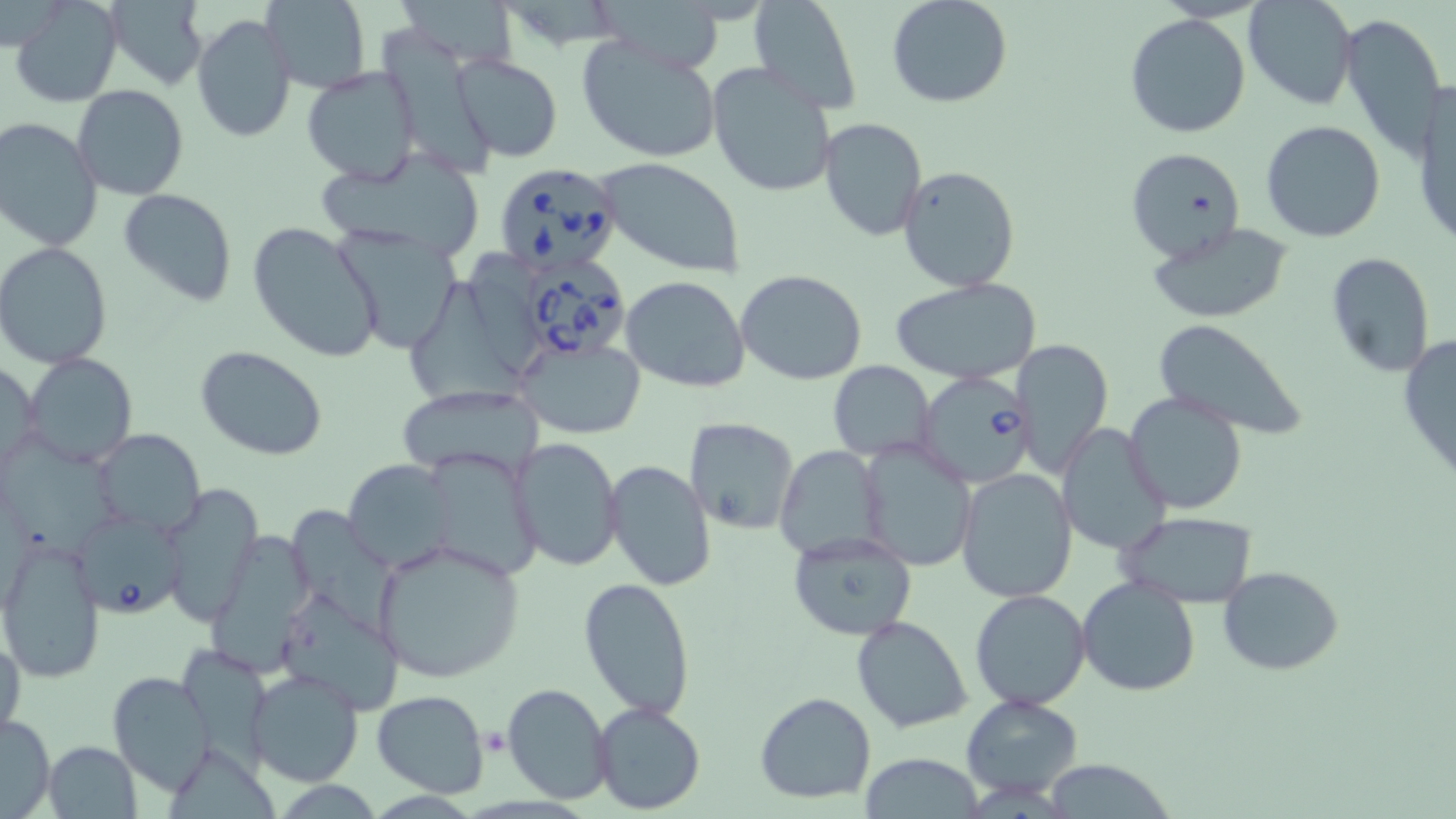
Babesia divergens-infected red blood cell locations = approximate bounding boxes as [x1, y1, x2, y2] in pixels: [493, 162, 625, 274], [521, 256, 638, 365], [914, 372, 1035, 489], [72, 511, 187, 619]
slide-level diagnosis = Babesia divergens
magnification = 1000x
image size = 1456×819 pixels
field of view = single
preparation = thin blood film
stain = May-Grünwald-Giemsa
uninfected red blood cell locations = approximate bounding boxes as [x1, y1, x2, y2] in pixels: [10, 0, 123, 107], [105, 0, 208, 90], [262, 0, 371, 94], [887, 0, 1013, 108], [1243, 1, 1357, 110], [749, 2, 861, 115], [600, 5, 725, 75], [1124, 12, 1252, 140], [1339, 12, 1446, 160], [191, 13, 296, 143], [383, 29, 499, 176], [577, 36, 723, 165], [450, 54, 562, 164], [707, 62, 838, 199], [300, 66, 421, 187], [1413, 80, 1455, 252], [72, 86, 190, 201], [0, 117, 104, 252], [819, 117, 927, 243], [1262, 119, 1385, 243], [1127, 146, 1246, 265], [314, 149, 489, 260], [598, 159, 748, 278], [897, 164, 1023, 293], [118, 189, 238, 307], [247, 221, 384, 364], [1145, 222, 1291, 322], [332, 227, 463, 355], [0, 242, 117, 369], [1324, 252, 1436, 376], [736, 270, 868, 385], [621, 275, 750, 391], [893, 277, 1039, 384], [404, 280, 521, 411], [1150, 318, 1308, 442], [1397, 331, 1456, 485], [517, 336, 646, 440], [1011, 338, 1113, 478], [194, 344, 330, 460], [23, 353, 138, 469], [827, 361, 936, 461], [0, 363, 41, 473], [403, 384, 536, 474], [1124, 391, 1251, 515], [684, 417, 799, 534], [1057, 422, 1172, 556], [4, 429, 118, 555], [95, 430, 205, 535], [511, 437, 625, 574], [860, 440, 977, 570], [775, 446, 888, 561], [423, 448, 548, 579], [343, 459, 459, 572], [604, 460, 716, 592], [955, 469, 1078, 603], [158, 483, 263, 625], [292, 505, 411, 646], [1117, 510, 1258, 606], [787, 532, 919, 642], [205, 534, 320, 678], [1, 536, 107, 681], [372, 539, 527, 683], [1218, 565, 1344, 674], [1077, 575, 1200, 696], [577, 576, 697, 720], [279, 586, 400, 724], [970, 590, 1091, 710], [850, 616, 973, 734], [0, 633, 26, 742], [177, 644, 273, 773], [246, 666, 363, 786], [107, 671, 216, 795], [503, 683, 612, 803], [372, 690, 490, 797], [754, 691, 875, 805], [960, 694, 1084, 801], [592, 701, 707, 815], [0, 712, 55, 818], [44, 740, 142, 819], [858, 755, 987, 817], [1044, 761, 1175, 819]
modality = optical microscopy
platelet locations = approximate bounding boxes as [x1, y1, x2, y2] in pixels: [482, 729, 511, 755]